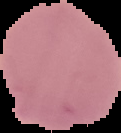
Image is 121×133 pixels. Malaria status: uninfected. From a thin blood film. Segmented cell region on a black background.